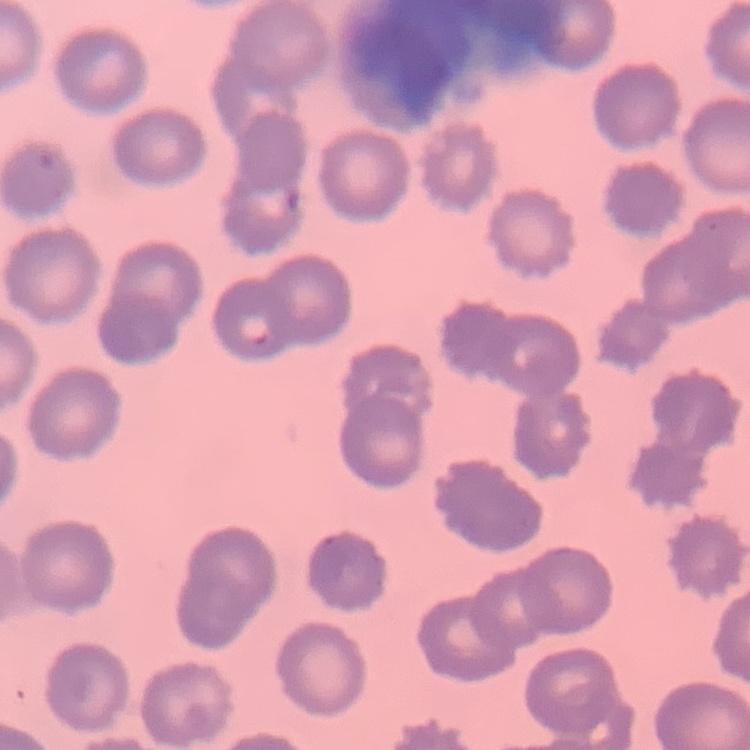

Summary:
  - Erythrocyte morphology: no rouleaux formation
  - Preparation: thin peripheral smear
  - Image type: square crop of a larger photomicrograph
  - Stain: Field's or Giemsa